Locate every blood parasite and identify its species.
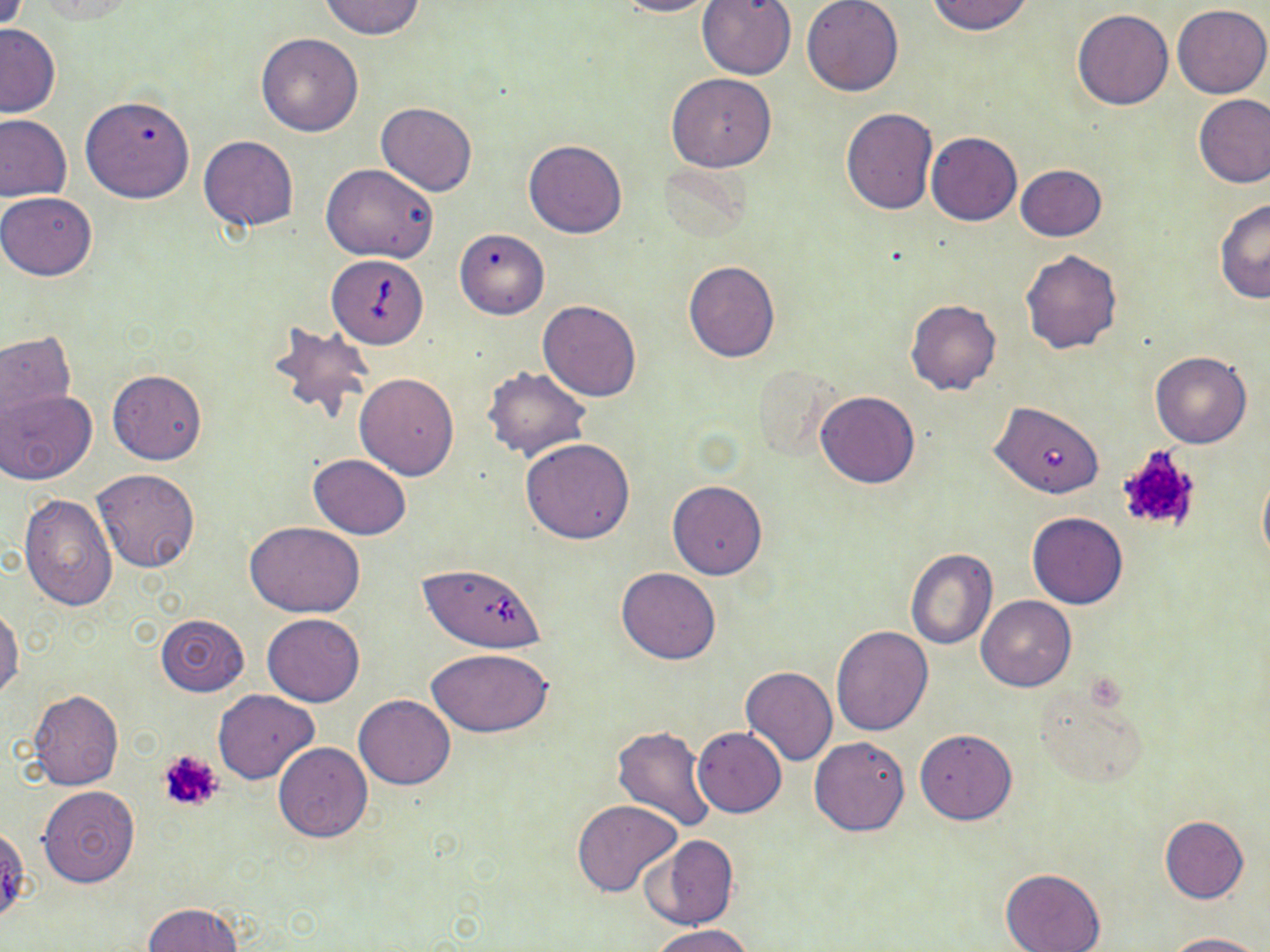
Approximate bounding boxes as (x1,y1)-(x2,y2) corner pairs in pixels.
Babesia divergens-infected red blood cells: (327,255)-(428,349), (986,401)-(1105,503), (417,563)-(546,653).
No Plasmodium falciparum, Plasmodium ovale, Plasmodium malariae, Plasmodium vivax, or Trypanosoma brucei observed.

slide-level diagnosis = Babesia divergens
image size = 1270×952 pixels
preparation = thin blood smear
magnification = 1000x
uninfected red blood cell locations = approximate bounding boxes as (x1,y1)-(x2,y2) corner pairs in pixels: (318,0)-(425,39), (616,0)-(720,18), (696,0)-(798,79), (927,0)-(1033,35), (33,1)-(140,22), (802,1)-(904,97), (1172,4)-(1270,99), (1071,8)-(1174,110), (0,23)-(60,117), (256,33)-(364,136), (666,72)-(776,172), (1193,93)-(1270,188), (80,95)-(193,204), (376,102)-(476,196), (840,107)-(938,214), (0,114)-(71,202), (926,132)-(1022,226), (199,135)-(299,232), (524,139)-(627,238), (322,164)-(439,263), (1015,165)-(1105,241), (0,192)-(97,281), (1214,199)-(1269,304), (454,227)-(549,319), (1020,249)-(1122,353), (683,261)-(781,363), (538,300)-(642,401), (906,300)-(1001,394), (267,320)-(375,423), (1,332)-(76,430), (1151,351)-(1251,448), (482,367)-(591,461), (108,369)-(206,464), (355,371)-(459,479), (3,389)-(96,485), (814,391)-(920,488), (521,438)-(635,543), (309,454)-(411,539), (92,467)-(201,573), (1257,467)-(1270,571), (668,481)-(768,580), (19,495)-(117,608), (1026,512)-(1128,608), (245,521)-(365,617), (904,548)-(997,649), (616,567)-(720,664), (975,595)-(1075,691), (0,606)-(22,701), (263,613)-(363,707), (156,614)-(249,696), (831,625)-(934,734), (428,649)-(553,737), (741,667)-(838,766), (1033,684)-(1148,789), (28,689)-(123,791), (213,689)-(317,784), (354,694)-(456,789), (613,725)-(715,832), (692,726)-(786,817), (916,729)-(1017,824), (810,737)-(910,836), (273,742)-(373,841), (38,785)-(140,887), (572,800)-(683,896), (1160,816)-(1248,903), (642,834)-(738,931), (1001,867)-(1105,952), (141,903)-(245,952), (651,924)-(756,952), (1162,932)-(1263,952)
stain = May-Grünwald-Giemsa
modality = optical microscopy
field of view = single
platelet locations = approximate bounding boxes as (x1,y1)-(x2,y2) corner pairs in pixels: (1112,445)-(1205,538), (158,750)-(224,814)